Give the position of every malaria parasite and every leukocyte.
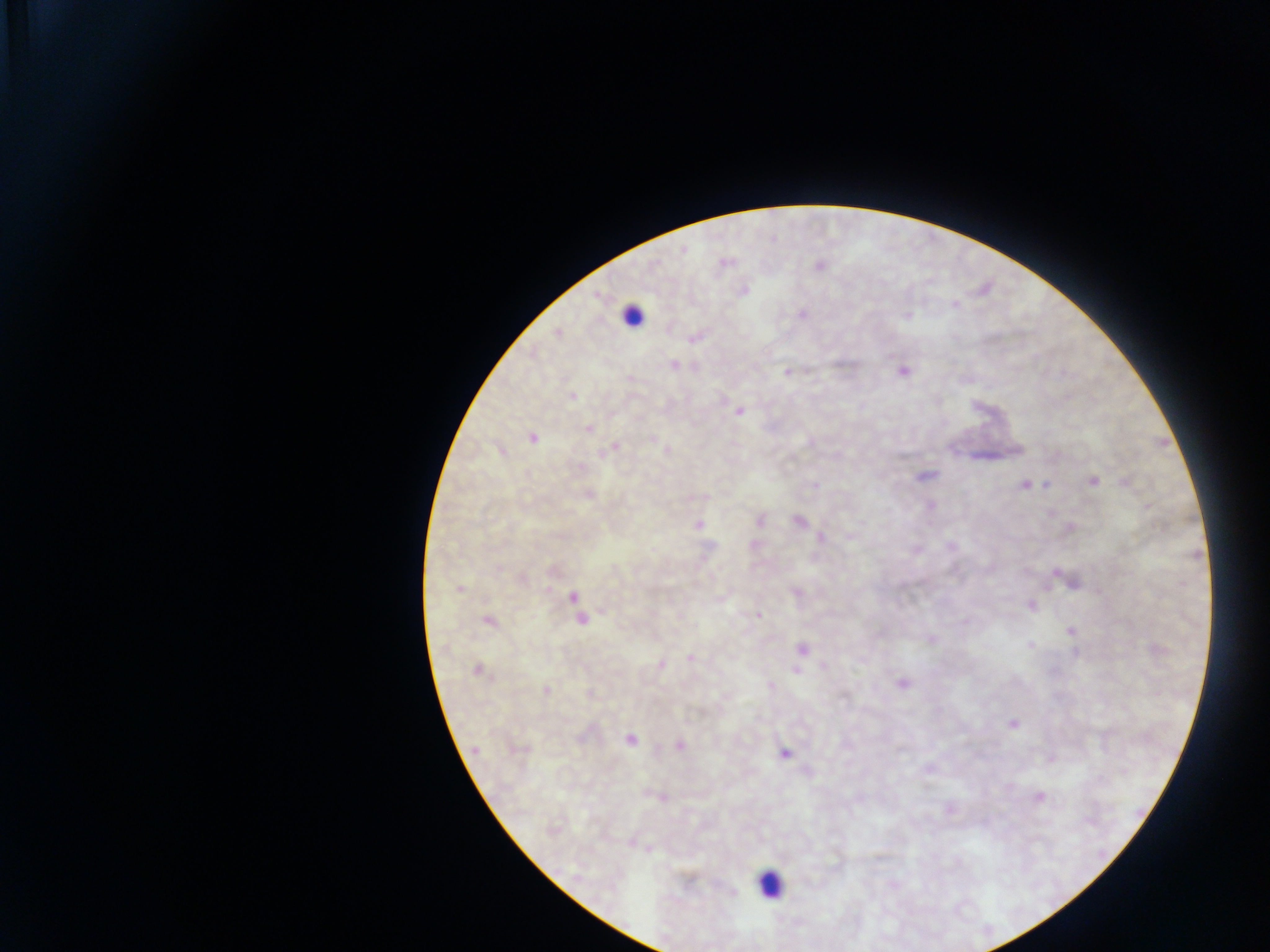
Approximate centers as x y in pixels.
Malaria parasites: 682 249; 724 263; 819 265; 743 290; 802 314; 907 315; 557 331; 695 337; 673 364; 902 369; 788 371; 571 395; 739 410; 588 428; 532 438; 615 448; 501 450; 667 451; 924 476; 1092 480; 1126 480; 1025 484; 1045 485; 588 495; 931 506; 759 519; 798 521; 698 526; 1070 528; 821 537; 1067 579; 459 589; 797 591; 574 597; 1030 605; 577 608; 757 614; 581 618; 488 620; 1071 631; 931 640; 1030 644; 801 648; 691 657; 660 664; 477 669; 796 670; 903 682; 545 690; 591 694; 1012 724; 630 739; 679 745; 474 750; 783 753; 1051 758; 660 795; 1038 796; 949 809.
Leukocytes: 631 316; 769 884.

Collected in Ghana. Image is 1270×952 pixels. Photographed through a microscope with a mobile-phone camera. Single field of view. Thick blood film.